Comment on the morphology of the red blood cells.
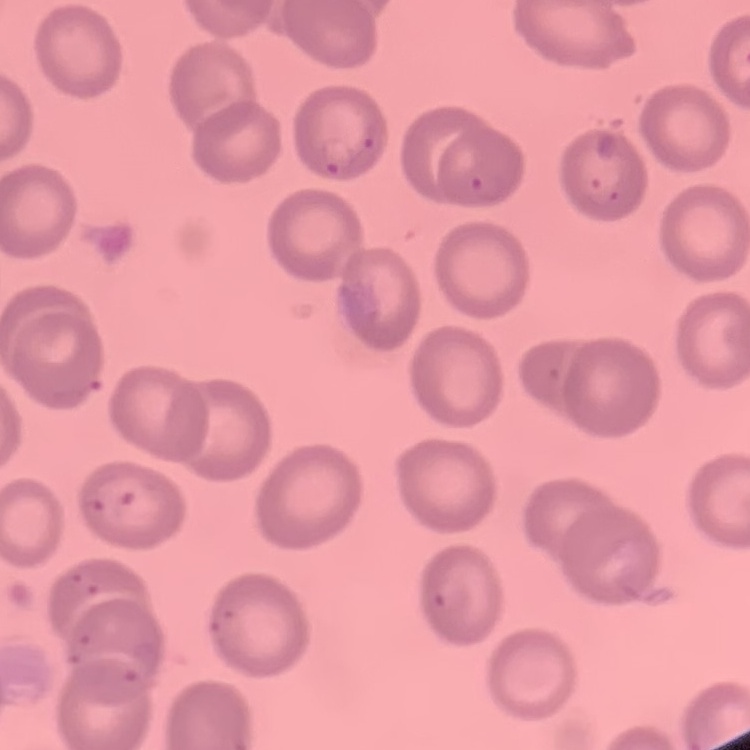

They show no rouleaux formation.

Square crop of a larger photomicrograph. Thin blood smear. Field's or Giemsa stain.